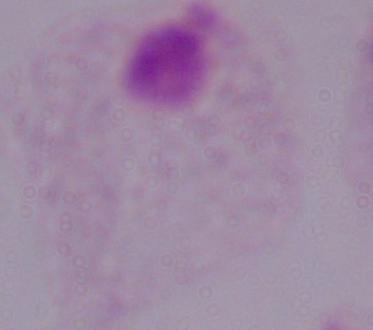
Photomicrograph. Captured at 1000x magnification. A trichomonad is seen.